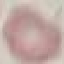
malaria status = uninfected
preparation = thin smear
capture = smartphone camera at the microscope eyepiece
image type = cell patch, automatically extracted from a larger field of view and resized to 64 × 64 pixels
stain = Giemsa